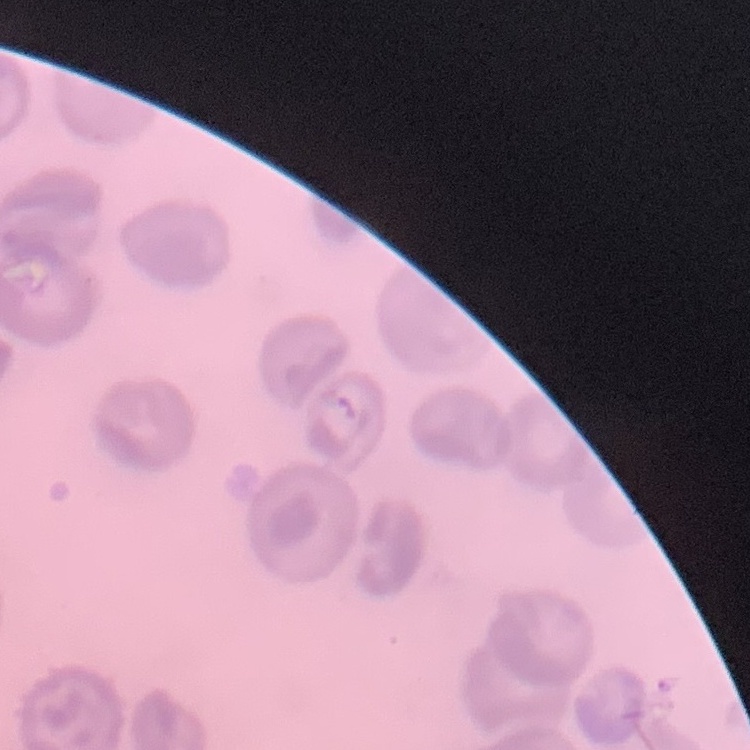
red_blood_cell_morphology: no rouleaux formation
stain: Field's or Giemsa
image_type: one tile cut from a larger photomicrograph
preparation: thin blood smear